Assess this cell for malaria.
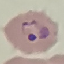

Parasitized.

Summary:
  - Preparation: thin blood smear
  - Capture: smartphone camera at the microscope eyepiece
  - Stain: Giemsa
  - Image type: cell patch, automatically extracted from a larger field of view and resized to 64 × 64 pixels